State the blood parasite species.
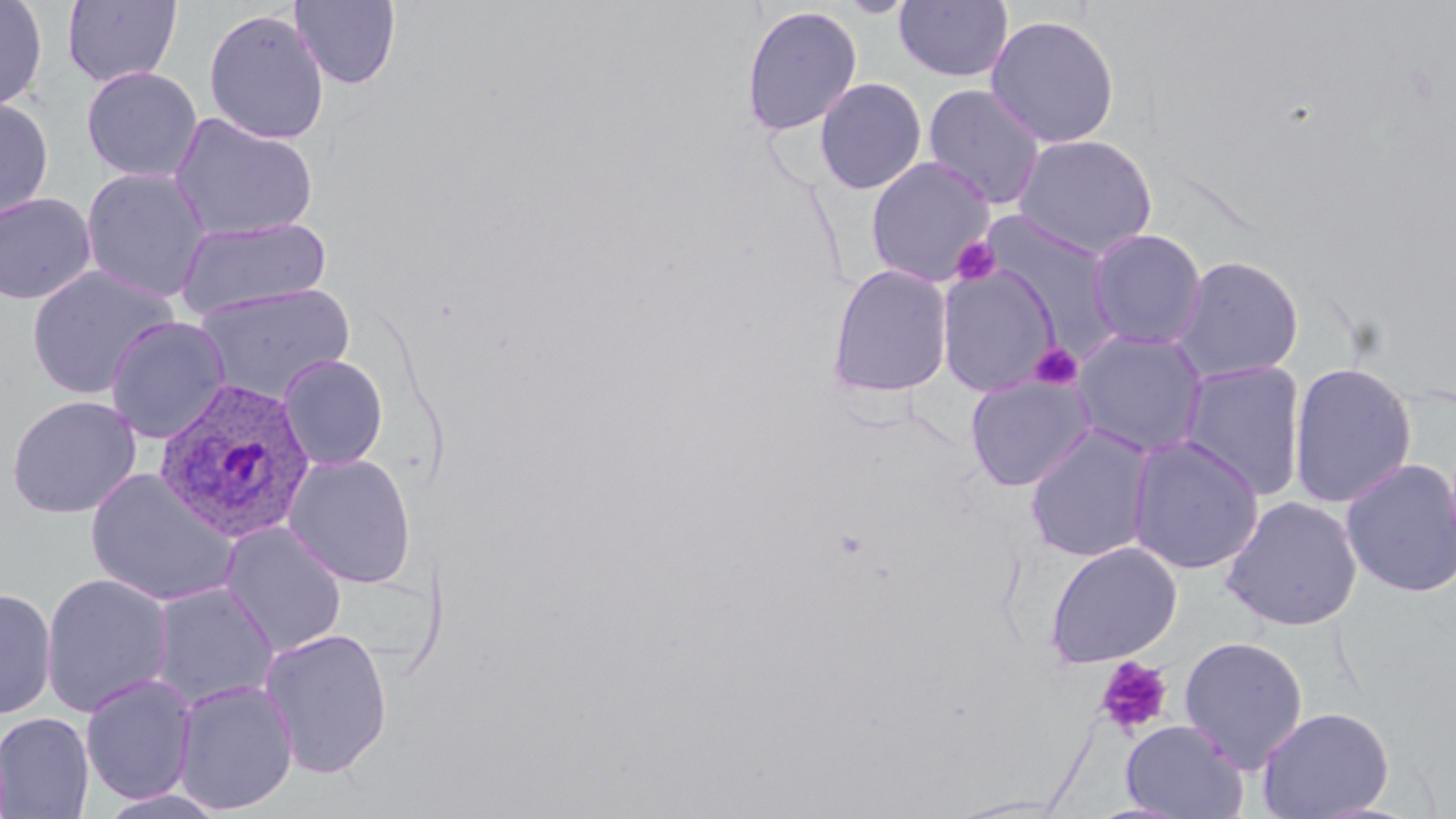
Plasmodium ovale.

{
  "modality": "light microscopy",
  "magnification": "1000x",
  "stain": "May-Grünwald-Giemsa",
  "uninfected_red_blood_cell_locations": "approximate bounding boxes as (x1,y1)-(x2,y2) corner pairs in pixels: (0,0)-(48,112), (290,0)-(401,91), (893,0)-(1014,84), (62,1)-(182,89), (740,5)-(863,137), (203,8)-(330,145), (985,13)-(1121,148), (80,65)-(203,182), (814,76)-(928,195), (922,83)-(1048,211), (0,97)-(54,223), (168,112)-(320,242), (1012,132)-(1159,259), (864,156)-(997,288), (80,167)-(212,303), (0,192)-(98,305), (985,212)-(1123,361), (175,215)-(333,321), (1086,228)-(1207,351), (1170,254)-(1306,383), (826,264)-(954,398), (936,264)-(1060,397), (26,265)-(180,401), (194,283)-(357,405), (105,316)-(230,443), (1071,329)-(1210,458), (277,354)-(389,471), (1178,360)-(1307,501), (1289,361)-(1418,509), (963,373)-(1097,491), (6,394)-(142,518), (1023,424)-(1158,564), (1127,434)-(1265,575), (283,453)-(418,589), (1340,458)-(1456,599), (85,468)-(239,607), (1220,495)-(1363,632), (220,521)-(347,658), (1044,540)-(1183,669), (41,573)-(174,717), (150,582)-(279,712), (0,587)-(58,719), (258,627)-(395,779), (1178,635)-(1309,772), (79,673)-(198,805), (172,678)-(299,814), (1256,705)-(1395,818), (0,711)-(95,819), (1119,719)-(1249,818), (96,788)-(230,818), (943,793)-(1075,817)",
  "image_size": "1456×819 pixels",
  "plasmodium_ovale_infected_red_blood_cell_locations": "approximate bounding boxes as (x1,y1)-(x2,y2) corner pairs in pixels: (154,377)-(317,544)",
  "platelet_locations": "approximate bounding boxes as (x1,y1)-(x2,y2) corner pairs in pixels: (953,237)-(1001,285), (1029,342)-(1083,392), (1095,656)-(1175,738)",
  "field_of_view": "one of a larger specimen",
  "preparation": "thin blood film"
}